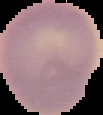 Image is 103×115 pixels. From a thin blood smear. Result: no malaria parasites seen. Segmented cell region on a black background.